State which parasite is depicted.
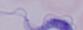

This is a trypanosome.

Captured at 1000x magnification. Photomicrograph.